Assess the morphology of the erythrocytes.
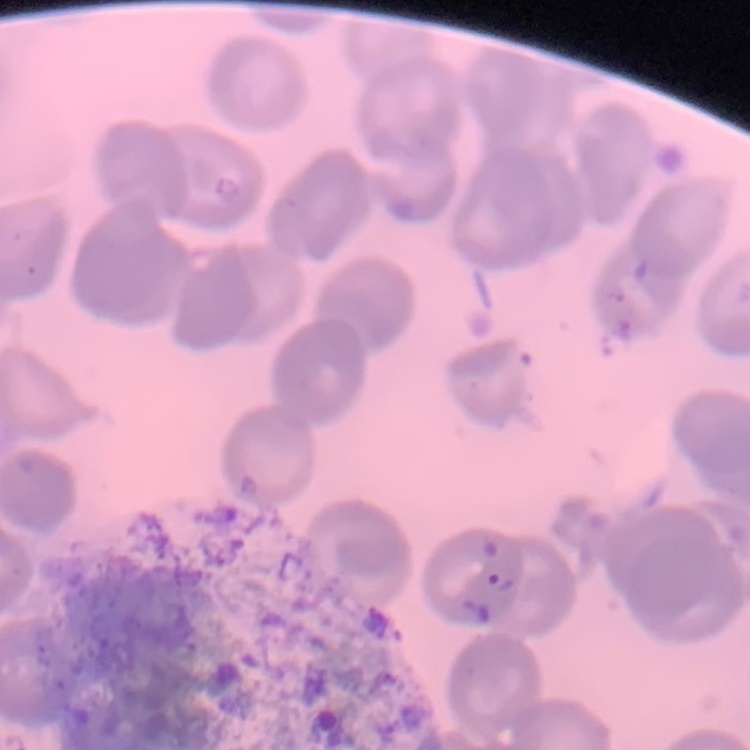
No rouleaux formation.

Summary:
  - Image type: one tile cut from a larger photomicrograph
  - Stain: Field's or Giemsa
  - Preparation: thin blood smear